Describe the morphology of the red blood cells.
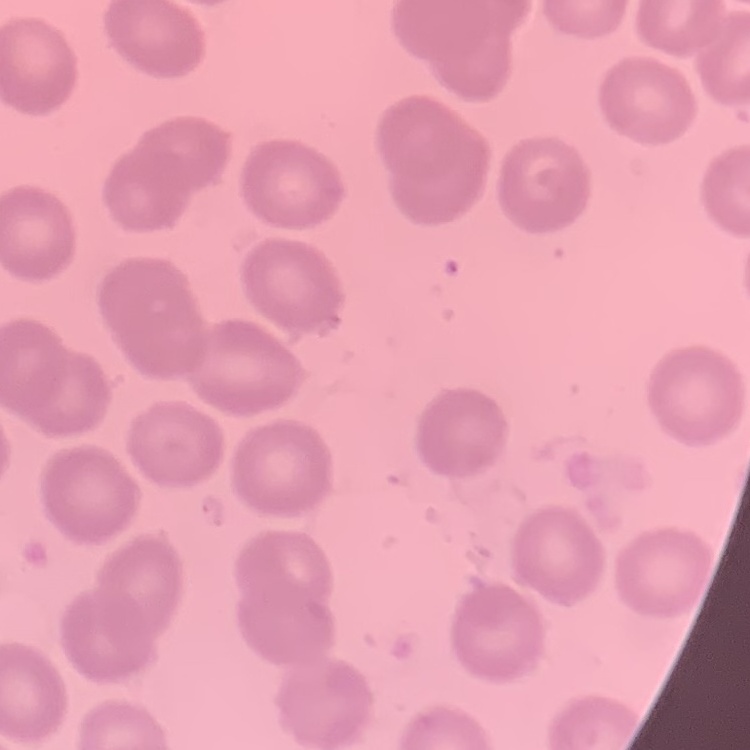

They show no rouleaux formation.

Summary:
  - Stain: Field's or Giemsa
  - Preparation: thin blood smear
  - Image type: one tile cut from a larger photomicrograph